Report the malaria status of this cell.
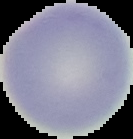
Uninfected.

{
  "image_size": "133×139 pixels",
  "image_type": "segmented cell region on a black background",
  "preparation": "thin blood film"
}